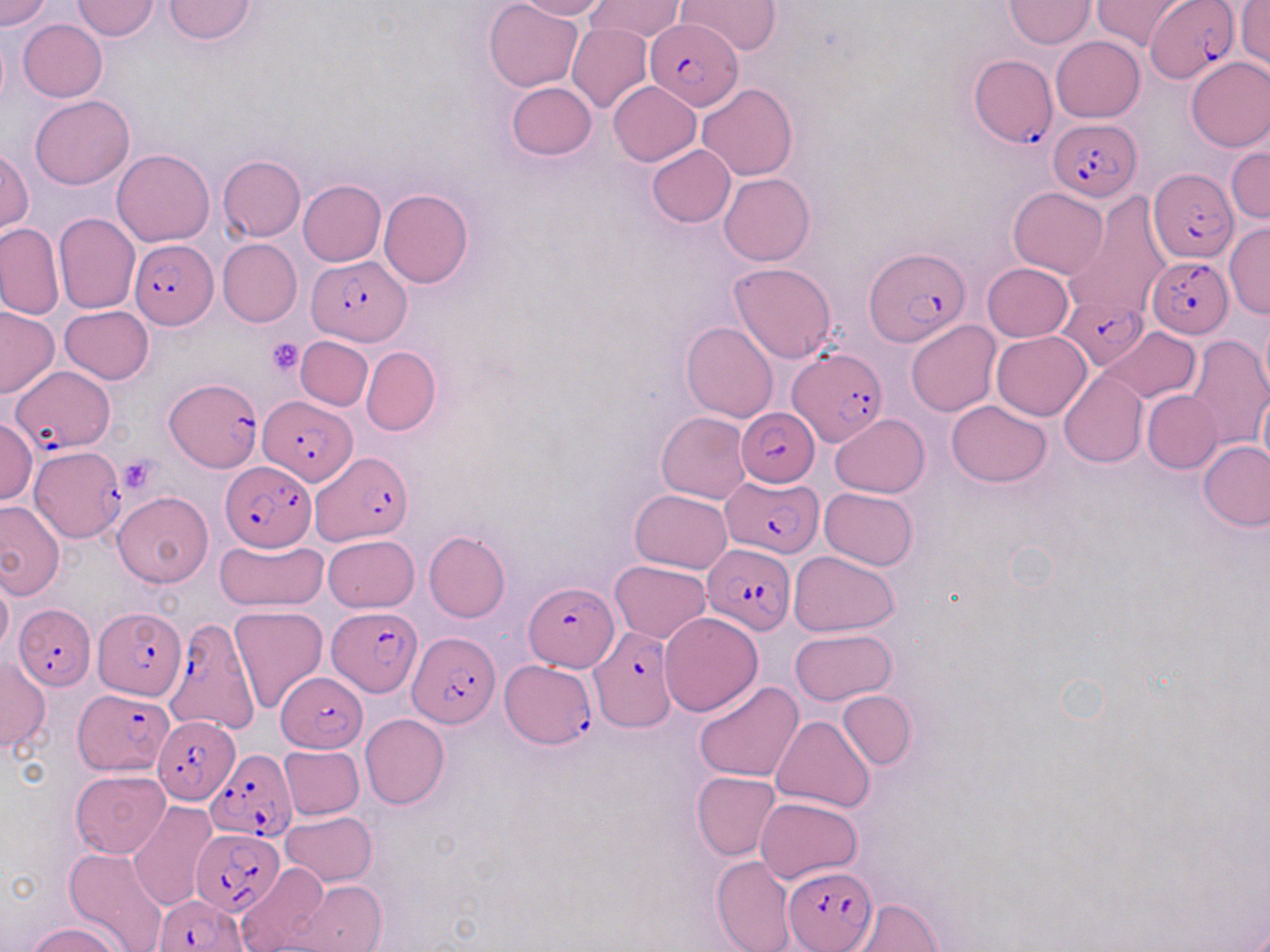 Approximate bounding boxes as (x1, y1, x2, y2) in pixels. Uninfected red blood cell locations (subset): (0, 0, 53, 31), (164, 0, 256, 43), (484, 0, 582, 91), (515, 0, 611, 20), (587, 0, 685, 44), (1004, 0, 1097, 48), (1091, 0, 1193, 49), (71, 1, 160, 40), (1236, 1, 1270, 70), (18, 18, 107, 102), (566, 22, 652, 114), (1051, 36, 1144, 122), (1184, 56, 1270, 152), (609, 81, 701, 165), (505, 82, 597, 161), (697, 82, 797, 180), (31, 95, 134, 190), (646, 145, 736, 227), (1226, 146, 1268, 225), (1, 149, 33, 234), (112, 149, 215, 247), (217, 154, 305, 241), (719, 173, 814, 265), (298, 180, 386, 266), (1009, 187, 1107, 277), (378, 188, 474, 288), (1063, 194, 1170, 322), (54, 212, 141, 313), (0, 223, 64, 320), (1222, 224, 1269, 318), (217, 238, 302, 326), (729, 263, 837, 364), (982, 263, 1073, 342), (0, 305, 58, 399), (59, 305, 154, 384), (1258, 311, 1270, 406), (905, 320, 1001, 416), (682, 321, 778, 423), (1101, 327, 1200, 402), (992, 331, 1091, 420), (1185, 334, 1269, 451), (296, 335, 373, 410), (362, 346, 440, 435), (1059, 369, 1149, 468), (1257, 382, 1270, 481), (1143, 391, 1222, 473), (946, 400, 1051, 487), (656, 412, 751, 503), (830, 413, 929, 497), (0, 419, 37, 504), (1198, 440, 1269, 531), (820, 488, 918, 571), (629, 489, 732, 574), (114, 491, 214, 587), (0, 501, 64, 599), (423, 531, 510, 622), (323, 534, 419, 612), (215, 538, 328, 612), (789, 551, 901, 637), (610, 559, 711, 642), (0, 575, 13, 656), (229, 605, 327, 712), (658, 611, 763, 717), (790, 628, 897, 705), (0, 657, 49, 753), (694, 680, 805, 783), (837, 691, 917, 769), (359, 714, 450, 810), (770, 716, 875, 813), (279, 744, 364, 820), (72, 771, 170, 858), (692, 771, 781, 860), (756, 796, 862, 884), (127, 801, 216, 911), (280, 810, 378, 886), (64, 847, 169, 952), (710, 854, 796, 952), (237, 863, 330, 952), (291, 880, 387, 952), (842, 898, 943, 951), (27, 923, 125, 952). Plasmodium falciparum-infected red blood cell locations (subset): (1147, 2, 1237, 84), (645, 18, 742, 110), (969, 56, 1056, 147), (1049, 117, 1142, 200), (1149, 168, 1238, 261), (129, 239, 219, 330), (863, 249, 969, 345), (306, 255, 412, 345), (1148, 258, 1233, 340), (1058, 298, 1149, 370), (787, 347, 885, 447), (10, 365, 118, 453), (166, 378, 261, 471), (260, 395, 354, 481), (735, 408, 820, 487), (29, 447, 125, 540), (312, 452, 412, 545), (220, 460, 317, 551), (723, 476, 824, 559), (703, 543, 796, 635), (523, 581, 616, 671), (14, 603, 95, 689), (327, 606, 423, 696), (93, 608, 187, 700), (166, 616, 257, 729), (584, 624, 678, 732), (407, 631, 500, 728), (500, 661, 594, 749), (274, 669, 368, 752), (72, 689, 173, 774), (152, 716, 239, 805), (205, 750, 296, 841), (191, 829, 286, 916), (783, 866, 877, 952), (154, 894, 247, 952). Platelet locations: (265, 337, 305, 375), (118, 457, 159, 494). Slide-level diagnosis: Plasmodium falciparum. Single field of view. 1000x magnification. Thin blood film. May-Grünwald-Giemsa stain. Image is 1270×952 pixels. Light microscopy.